Outline each blood parasite and name the species.
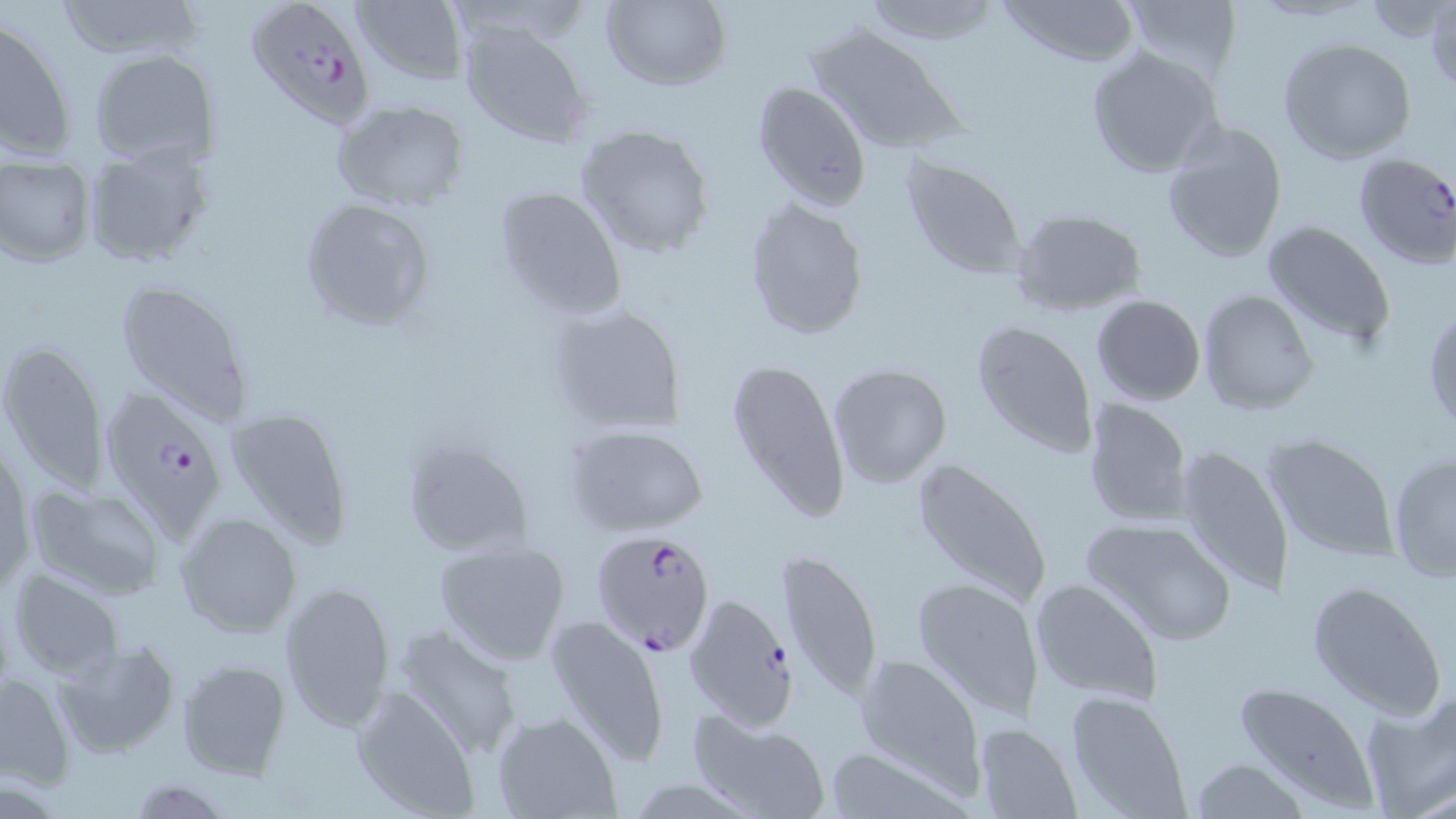

Approximate bounding boxes as (x1,y1)-(x2,y2) corner pairs in pixels.
Plasmodium falciparum-infected red blood cells: (248,0)-(373,128), (1350,152)-(1456,269), (98,384)-(229,540), (590,528)-(717,656), (683,593)-(797,730).
No Plasmodium ovale, Plasmodium malariae, Plasmodium vivax, Babesia divergens, or Trypanosoma brucei observed.

Uninfected red blood cell locations: (55,0)-(207,61), (601,0)-(732,91), (861,0)-(1000,44), (997,0)-(1141,70), (1117,0)-(1244,85), (351,1)-(468,86), (1360,1)-(1454,41), (1425,1)-(1455,95), (459,16)-(595,151), (0,17)-(75,162), (806,24)-(960,155), (1278,37)-(1416,164), (1084,46)-(1223,179), (88,48)-(220,167), (752,80)-(872,210), (331,99)-(470,212), (1160,120)-(1289,263), (573,125)-(716,260), (79,141)-(217,269), (0,154)-(96,269), (903,158)-(1028,280), (492,184)-(629,321), (297,197)-(438,333), (743,197)-(869,340), (1009,207)-(1148,318), (1262,219)-(1397,351), (115,276)-(255,423), (1196,289)-(1320,416), (1091,295)-(1205,406), (544,302)-(685,436), (1425,305)-(1455,436), (972,319)-(1098,459), (1,339)-(110,493), (727,354)-(852,525), (828,361)-(952,488), (1081,397)-(1194,526), (225,406)-(353,548), (562,422)-(711,537), (1261,433)-(1400,562), (399,435)-(534,561), (1172,444)-(1294,593), (1385,450)-(1456,582), (907,452)-(1056,612), (25,483)-(168,600), (174,511)-(301,639), (1081,516)-(1241,648), (433,539)-(572,666), (775,546)-(883,704), (9,569)-(125,680), (909,574)-(1046,720), (1028,577)-(1166,706), (279,579)-(396,735), (1304,580)-(1445,719), (546,614)-(671,767), (392,622)-(525,759), (53,640)-(181,758), (852,651)-(986,787), (178,661)-(293,780), (0,674)-(74,786), (1230,681)-(1384,808), (352,685)-(481,816), (1063,688)-(1192,819), (1361,692)-(1456,815), (688,707)-(831,818), (493,712)-(619,818), (973,722)-(1082,818), (821,741)-(973,817), (1190,758)-(1310,818), (126,778)-(232,816). Slide-level diagnosis: Plasmodium falciparum. May-Grünwald-Giemsa stain. Captured at 1000x magnification. Light microscopy. Image is 1456×819 pixels. Thin blood smear. One field of a larger specimen.